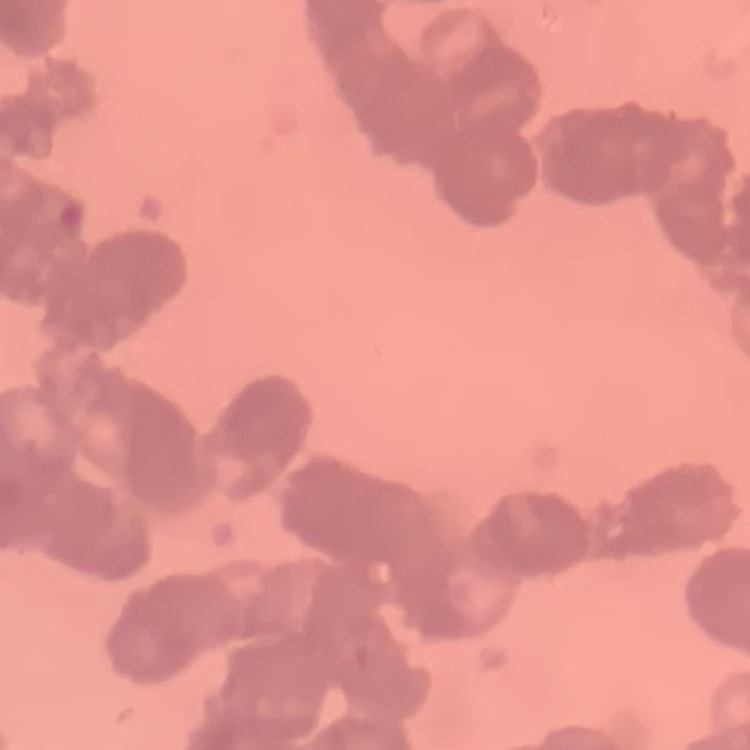
erythrocyte morphology = rouleaux formation
stain = Field's or Giemsa
preparation = thin blood smear
image type = one tile cut from a larger photomicrograph